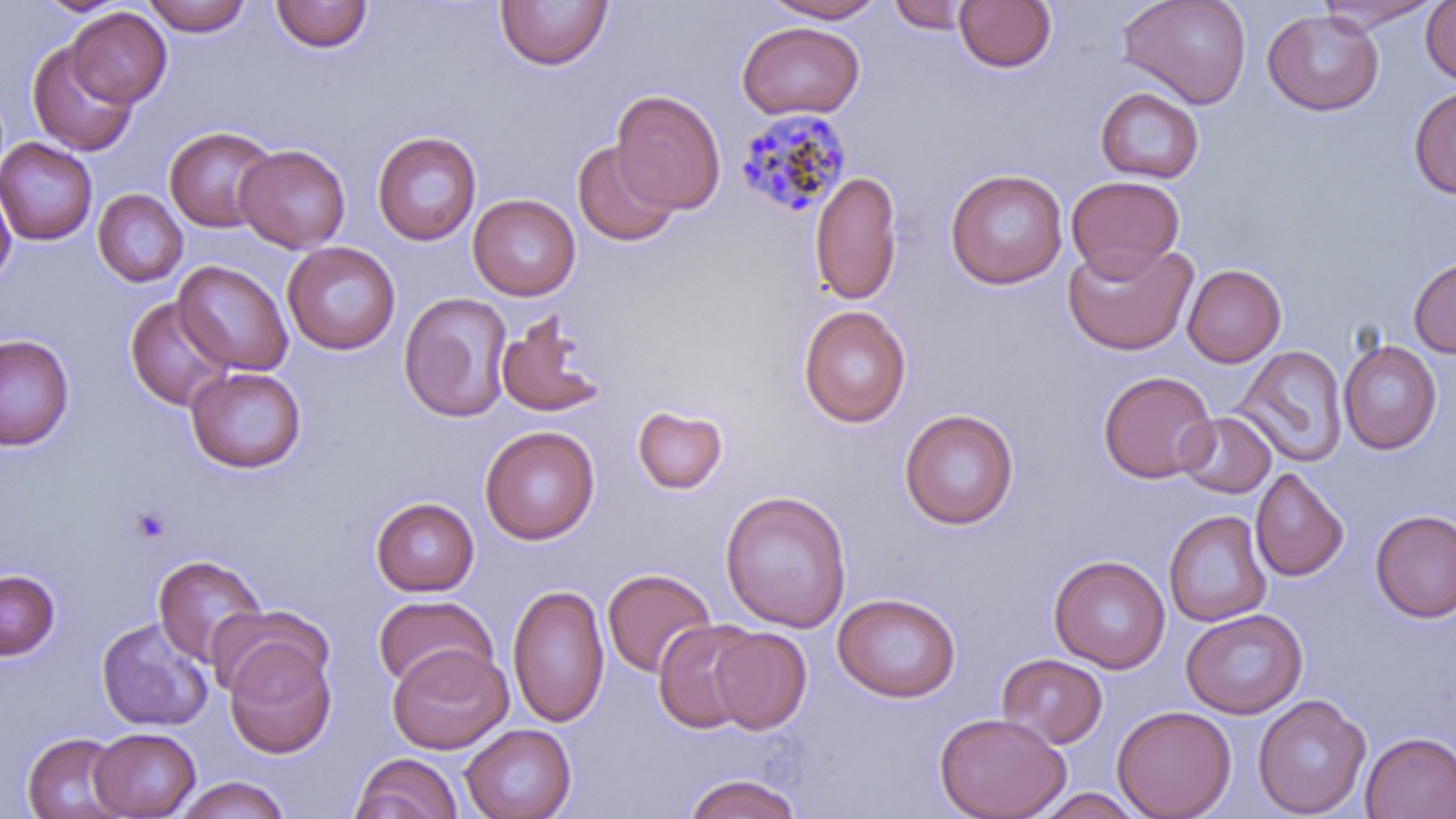

slide_level_diagnosis: Plasmodium malariae
field_of_view: single
image_size: 1456×819 pixels
magnification: 1000x
modality: optical microscopy
platelet_locations: 'approximate bounding boxes as named x1/y1/x2/y2 corners in pixels: (x1=127, y1=504, x2=174, y2=545)'
preparation: thin blood smear
plasmodium_malariae_infected_red_blood_cell_locations: 'approximate bounding boxes as named x1/y1/x2/y2 corners in pixels: (x1=733, y1=107, x2=852, y2=220)'
uninfected_red_blood_cell_locations: 'approximate bounding boxes as named x1/y1/x2/y2 corners in pixels: (x1=34, y1=0, x2=131, y2=17), (x1=141, y1=0, x2=253, y2=36), (x1=495, y1=0, x2=613, y2=71), (x1=763, y1=0, x2=886, y2=23), (x1=954, y1=0, x2=1056, y2=73), (x1=1117, y1=0, x2=1252, y2=110), (x1=1421, y1=0, x2=1456, y2=86), (x1=270, y1=1, x2=372, y2=53), (x1=887, y1=1, x2=974, y2=34), (x1=1315, y1=1, x2=1444, y2=33), (x1=66, y1=7, x2=171, y2=107), (x1=1262, y1=9, x2=1384, y2=115), (x1=737, y1=21, x2=864, y2=120), (x1=26, y1=40, x2=139, y2=157), (x1=1409, y1=86, x2=1456, y2=199), (x1=1094, y1=87, x2=1204, y2=185), (x1=611, y1=90, x2=726, y2=213), (x1=164, y1=126, x2=279, y2=232), (x1=371, y1=131, x2=482, y2=245), (x1=0, y1=138, x2=98, y2=246), (x1=572, y1=141, x2=680, y2=247), (x1=234, y1=144, x2=350, y2=253), (x1=944, y1=169, x2=1068, y2=289), (x1=809, y1=172, x2=902, y2=305), (x1=0, y1=175, x2=17, y2=289), (x1=1066, y1=175, x2=1184, y2=279), (x1=92, y1=189, x2=188, y2=287), (x1=468, y1=193, x2=581, y2=301), (x1=1062, y1=240, x2=1197, y2=356), (x1=282, y1=242, x2=400, y2=355), (x1=1409, y1=257, x2=1456, y2=358), (x1=172, y1=260, x2=293, y2=376), (x1=1182, y1=264, x2=1286, y2=367), (x1=399, y1=292, x2=512, y2=422), (x1=123, y1=296, x2=234, y2=412), (x1=798, y1=305, x2=911, y2=427), (x1=495, y1=309, x2=608, y2=418), (x1=0, y1=334, x2=75, y2=450), (x1=1338, y1=339, x2=1442, y2=454), (x1=1234, y1=346, x2=1347, y2=467), (x1=185, y1=366, x2=307, y2=473), (x1=1098, y1=370, x2=1217, y2=484), (x1=631, y1=403, x2=730, y2=495), (x1=899, y1=409, x2=1019, y2=530), (x1=1177, y1=411, x2=1277, y2=500), (x1=480, y1=426, x2=599, y2=544), (x1=1250, y1=468, x2=1349, y2=581), (x1=719, y1=489, x2=852, y2=632), (x1=370, y1=497, x2=480, y2=596), (x1=1370, y1=510, x2=1456, y2=623), (x1=1163, y1=511, x2=1272, y2=627), (x1=153, y1=554, x2=266, y2=667), (x1=1049, y1=555, x2=1170, y2=674), (x1=602, y1=568, x2=716, y2=678), (x1=0, y1=570, x2=60, y2=660), (x1=507, y1=584, x2=609, y2=728), (x1=832, y1=593, x2=961, y2=703), (x1=372, y1=595, x2=497, y2=692), (x1=207, y1=605, x2=331, y2=702), (x1=1180, y1=608, x2=1308, y2=719), (x1=95, y1=616, x2=214, y2=733), (x1=653, y1=619, x2=761, y2=734), (x1=708, y1=627, x2=812, y2=734), (x1=224, y1=639, x2=336, y2=759), (x1=387, y1=645, x2=512, y2=754), (x1=997, y1=653, x2=1108, y2=750), (x1=1252, y1=694, x2=1370, y2=818), (x1=1112, y1=705, x2=1236, y2=819), (x1=933, y1=712, x2=1071, y2=819), (x1=461, y1=724, x2=576, y2=819), (x1=90, y1=727, x2=201, y2=817), (x1=22, y1=732, x2=129, y2=819), (x1=1359, y1=732, x2=1456, y2=818), (x1=350, y1=753, x2=462, y2=819), (x1=684, y1=773, x2=801, y2=819), (x1=173, y1=776, x2=291, y2=819), (x1=1031, y1=788, x2=1144, y2=818)'
stain: May-Grünwald-Giemsa